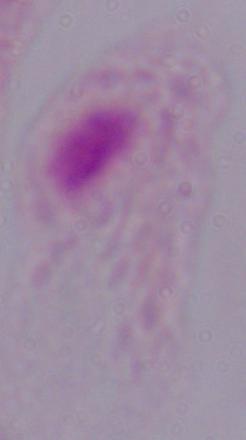
1000x magnification. A trichomonad is shown. Photomicrograph.